Assess this cell for malaria.
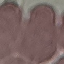
It is uninfected.

capture = smartphone camera at the microscope eyepiece
image type = automatically extracted cell patch, resized to 64 × 64 pixels
stain = Giemsa
preparation = thin smear